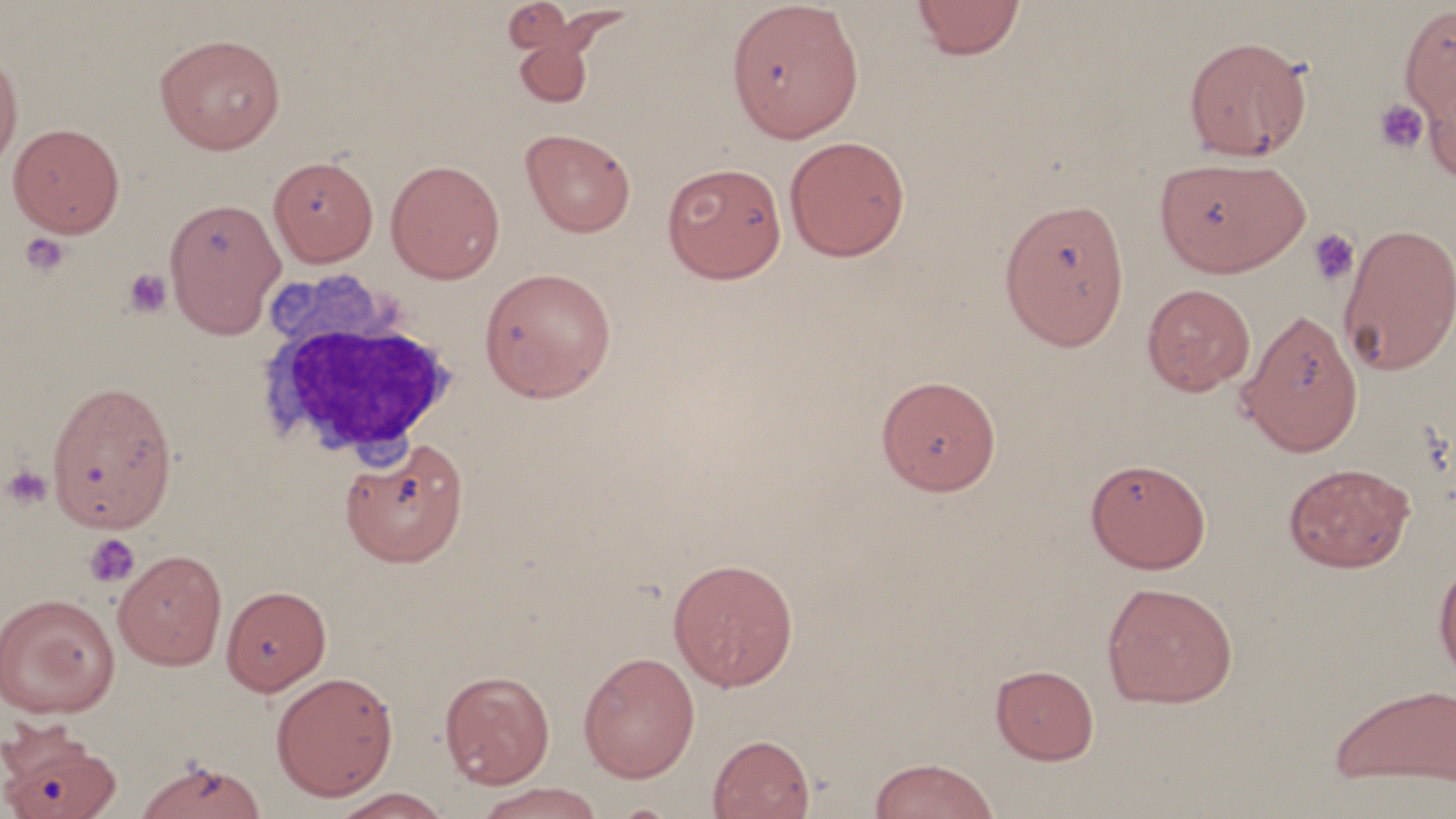
Approximate bounding boxes as (x1, y1, x2, y2) in pixels. Platelet locations: (1373, 99, 1430, 154), (1307, 228, 1360, 287), (19, 231, 71, 277), (123, 268, 172, 318), (2, 464, 53, 509), (84, 533, 141, 589). Uninfected red blood cell locations: (499, 0, 628, 110), (726, 0, 865, 143), (911, 0, 1026, 60), (1399, 3, 1456, 125), (154, 33, 286, 154), (1184, 35, 1313, 161), (0, 48, 23, 173), (1422, 63, 1456, 183), (8, 122, 125, 237), (520, 128, 635, 238), (784, 135, 911, 262), (1153, 155, 1311, 277), (268, 156, 378, 266), (385, 159, 505, 284), (661, 162, 788, 284), (163, 196, 286, 337), (998, 198, 1131, 351), (1338, 222, 1456, 376), (478, 266, 616, 402), (1141, 283, 1256, 396), (1237, 307, 1364, 457), (876, 375, 1002, 495), (46, 378, 179, 535), (339, 437, 469, 567), (1085, 458, 1211, 574), (1283, 462, 1416, 572), (113, 549, 228, 670), (1433, 554, 1456, 682), (667, 557, 800, 692), (1101, 582, 1238, 708), (222, 586, 331, 696), (0, 592, 120, 718), (578, 651, 700, 782), (991, 663, 1099, 765), (440, 669, 555, 789), (270, 670, 398, 802), (1329, 683, 1456, 788), (0, 728, 121, 819), (707, 734, 815, 819), (132, 756, 268, 819), (869, 758, 999, 819), (473, 782, 606, 818), (329, 788, 452, 818). White blood cell locations: (252, 281, 466, 467). Slide-level diagnosis: negative for blood parasites. Light microscopy. Thin blood smear. Captured at 1000x magnification. May-Grünwald-Giemsa-stained preparation. Image is 1456×819 pixels. Single field of view.